Classify this cell by malaria status.
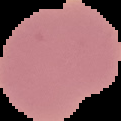

It is uninfected.

image type = cell region segmented out of the field of view; surrounding area masked to black
image size = 121×121 pixels
preparation = thin blood smear